Identify the preparation type.
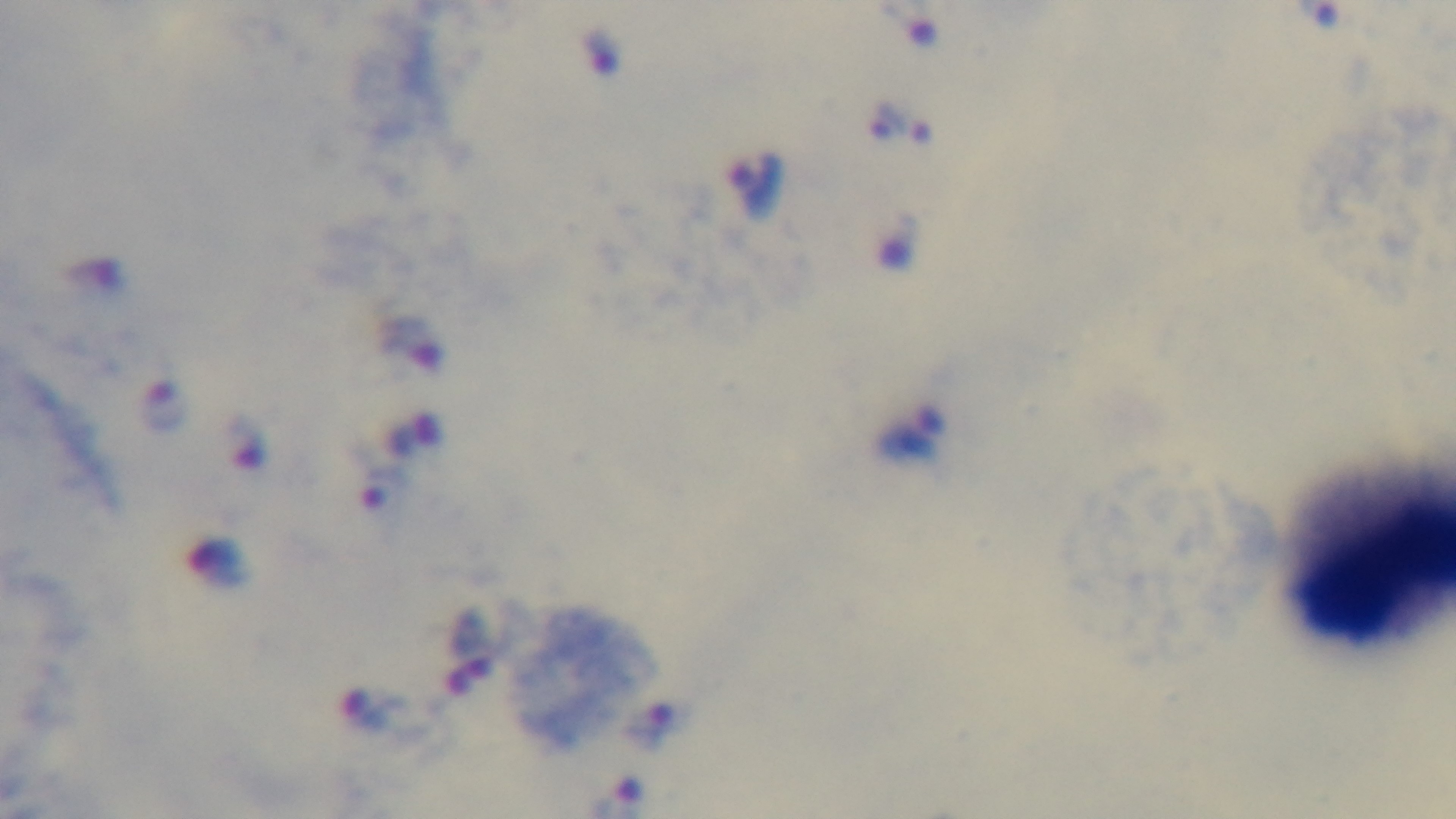

A thick smear.

Summary:
  - Malaria status: positive
  - Stain: Giemsa
  - Modality: light microscopy
  - Objective: 100x oil immersion
  - Field of view: single
  - Capture: mounted 4K digital camera